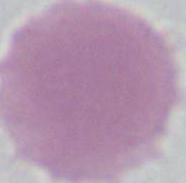
magnification: 1000x
modality: photomicrograph
identification: erythrocyte